Identify the parasite.
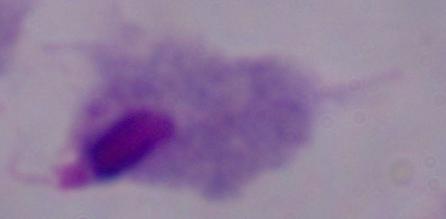

A trichomonad.

Summary:
  - Modality: micrograph
  - Magnification: 1000x